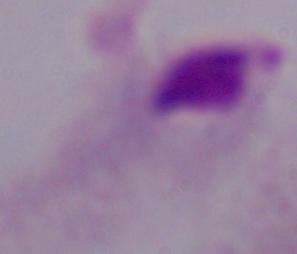 Captured at 1000x magnification. Micrograph. A trichomonad is shown.